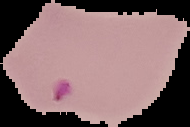
preparation = thin blood smear
image type = cell region segmented out of the field of view; surrounding area masked to black
result = malaria parasites detected
image size = 190×127 pixels